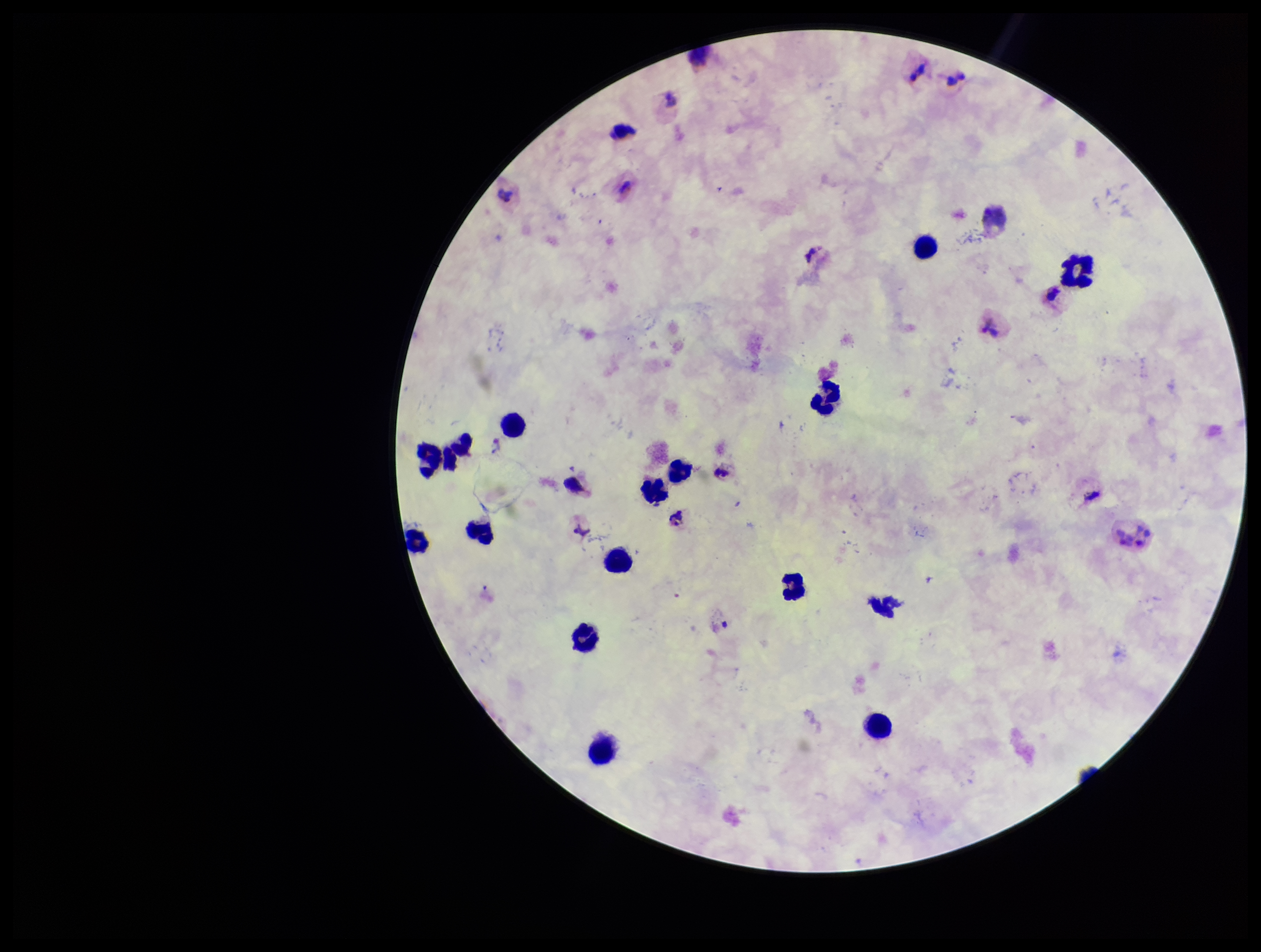
Species reported for this patient: Plasmodium vivax. Image is 1261×952 pixels. Plasmodium parasites: detected. Leukocyte count: 15. Parasite count: 3. Preparation: thick blood smear. Giemsa stain. Smartphone photograph taken through the eyepiece of a microscope. One field from this slide. Patient malaria status: positive.